Describe the morphology of the erythrocytes.
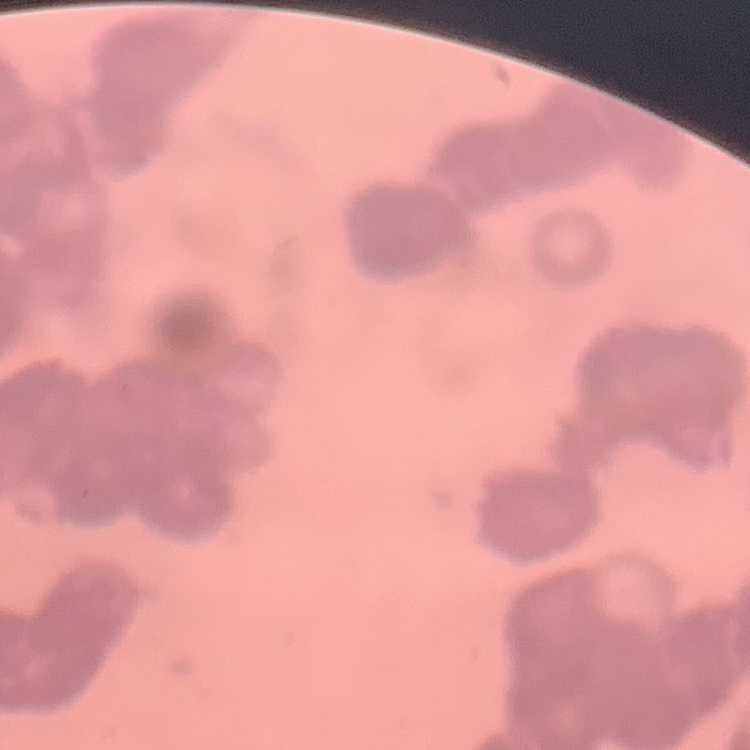
They show rouleaux formation.

One tile cut from a larger photomicrograph. Thin peripheral smear. Field's or Giemsa stain.